Assess this cell for malaria.
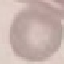

Uninfected.

Cell patch, automatically extracted from a larger field of view and resized to 64 × 64 pixels. Giemsa-stained preparation. Photographed with a smartphone camera at the microscope eyepiece. Thin smear of blood.